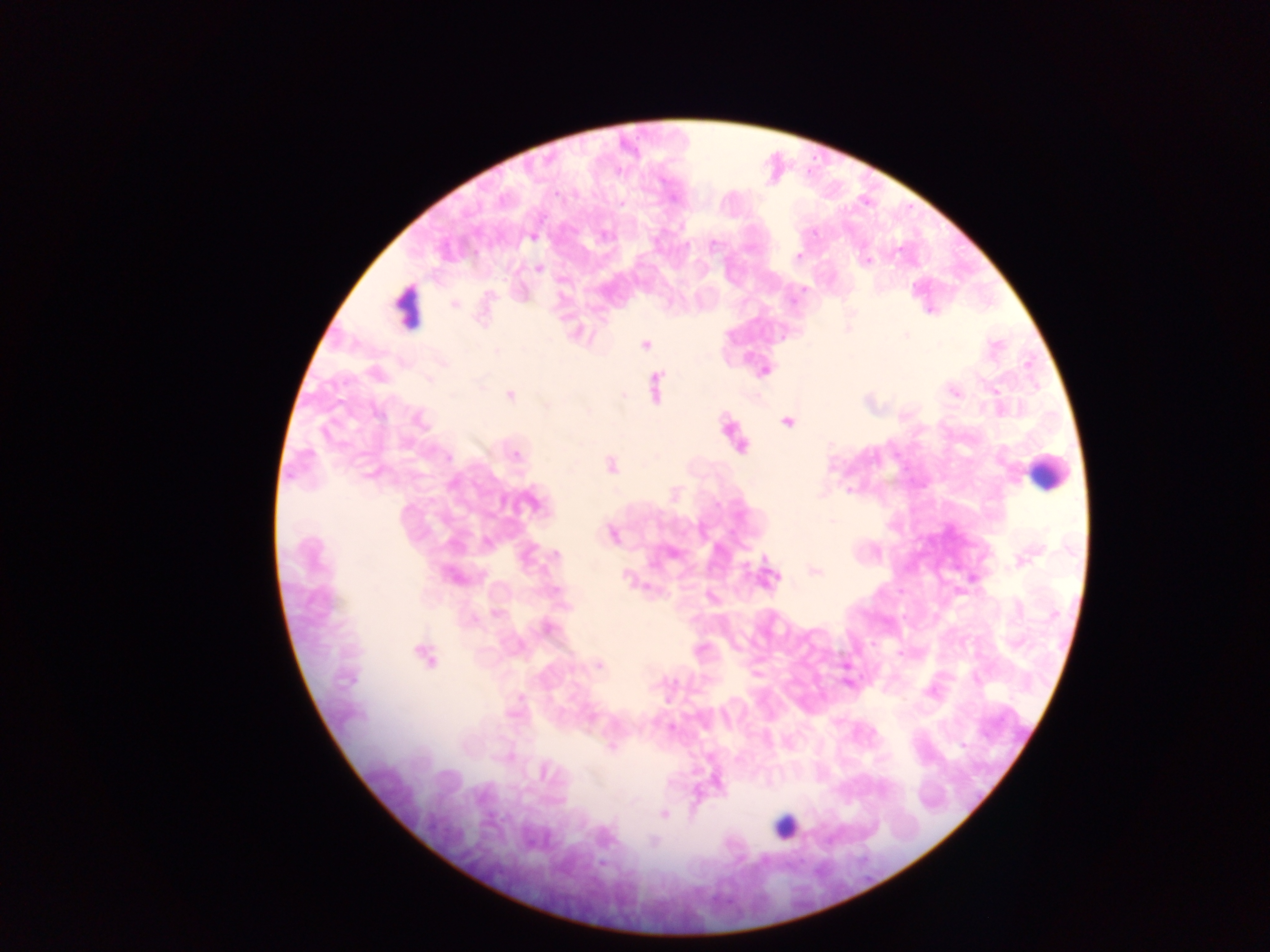
Approximate centers as (x, y) in pixels. Object labeled both malaria parasite and leukocyte by the source: (406, 308). Leukocyte locations: (1047, 472), (784, 827). Malaria parasite locations: (534, 237), (714, 245), (797, 255), (867, 261), (538, 268), (804, 288), (454, 304), (907, 336), (646, 344), (496, 351), (765, 371), (428, 379), (655, 387), (954, 391), (510, 395), (624, 396), (546, 404), (378, 414), (419, 420), (787, 422), (740, 446), (515, 454), (448, 457), (610, 466), (532, 503), (833, 521), (611, 534), (556, 555), (1023, 559), (816, 571), (452, 576), (626, 577), (770, 578), (497, 613), (547, 628), (424, 654), (599, 665), (512, 713), (962, 745), (610, 747), (545, 771), (663, 814), (653, 842), (602, 864). Image is 1270×952 pixels. Thick blood smear. Photographed through a microscope with a mobile-phone camera. Collected in Ghana. Single field of view.